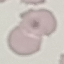

result = no malaria parasites seen
stain = Giemsa
image type = automatically extracted cell patch, resized to 64 × 64 pixels
capture = smartphone camera at the microscope eyepiece
preparation = thin blood smear